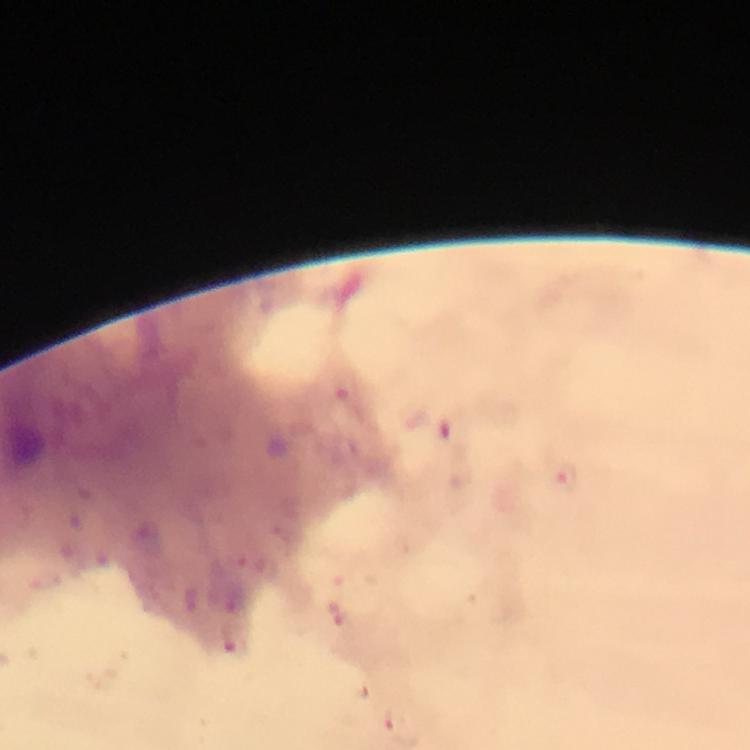
Approximate centers as (x, y) in pixels.
Summary:
  - Malaria parasite locations: (566, 481), (335, 614), (233, 645)
  - Capture: smartphone photograph through a microscope
  - Preparation: thick smear
  - Image size: 750×750 pixels
  - Magnification: 100x
  - Stain: Giemsa
  - Context: from a diagnostic examination for malaria
  - Immersion oil: applied
  - Cropped from: a single field of view